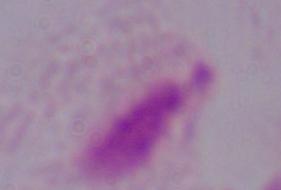

identification = trichomonad
magnification = 1000x
modality = micrograph